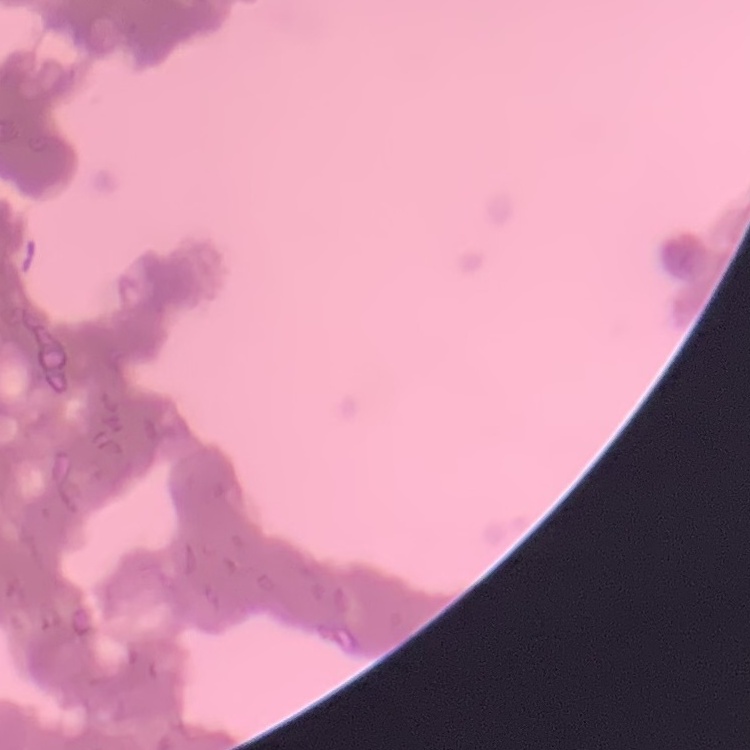
{
  "erythrocyte_morphology": "rouleaux formation",
  "preparation": "thin blood smear",
  "stain": "Field's or Giemsa",
  "image_type": "one tile cut from a larger photomicrograph"
}